Name the cell type shown.
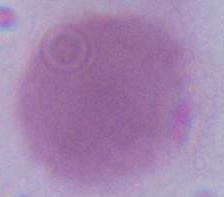

An erythrocyte.

magnification: 1000x
modality: photomicrograph